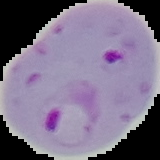

image size = 160×160 pixels
image type = segmented cell region with the area outside set to black
malaria status = parasitized
preparation = thin blood film